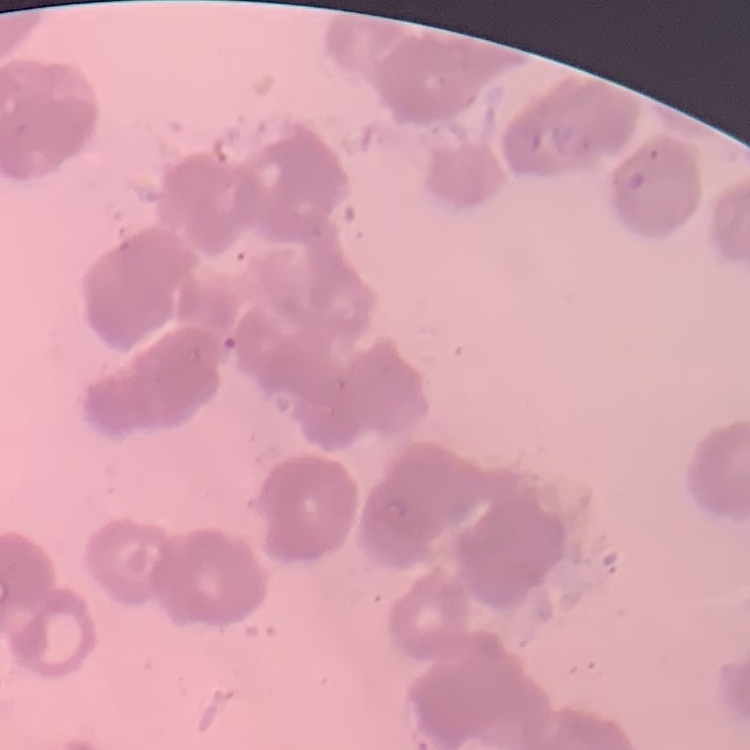
Summary:
  - Erythrocyte morphology: rouleaux formation
  - Image type: square crop of a larger photomicrograph
  - Stain: Field's or Giemsa
  - Preparation: thin blood film